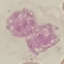
malaria status = uninfected
image type = cell patch, automatically extracted from a larger field of view and resized to 64 × 64 pixels
preparation = thin blood smear
stain = Giemsa
capture = smartphone camera at the microscope eyepiece